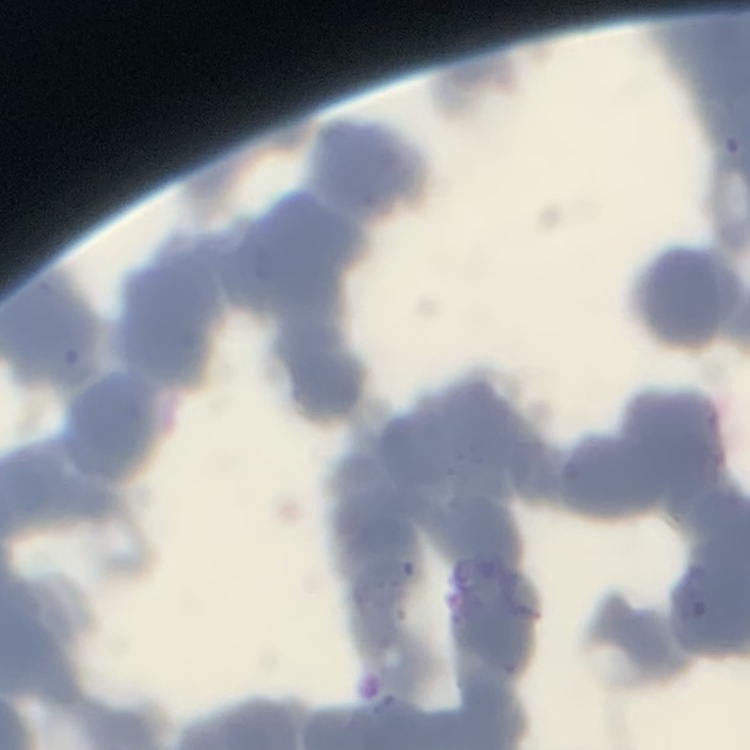

Summary:
  - Erythrocyte morphology: rouleaux formation
  - Image type: square crop of a larger photomicrograph
  - Preparation: thin peripheral smear
  - Stain: Field's or Giemsa